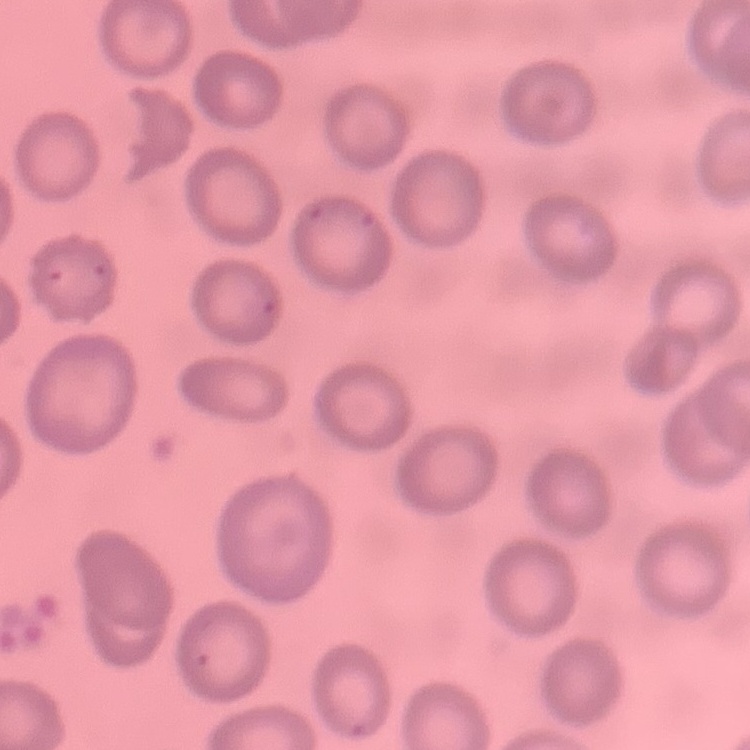

The erythrocytes exhibit no rouleaux formation. Thin blood film. Stained with either Field's or Giemsa. One tile cut from a larger photomicrograph.